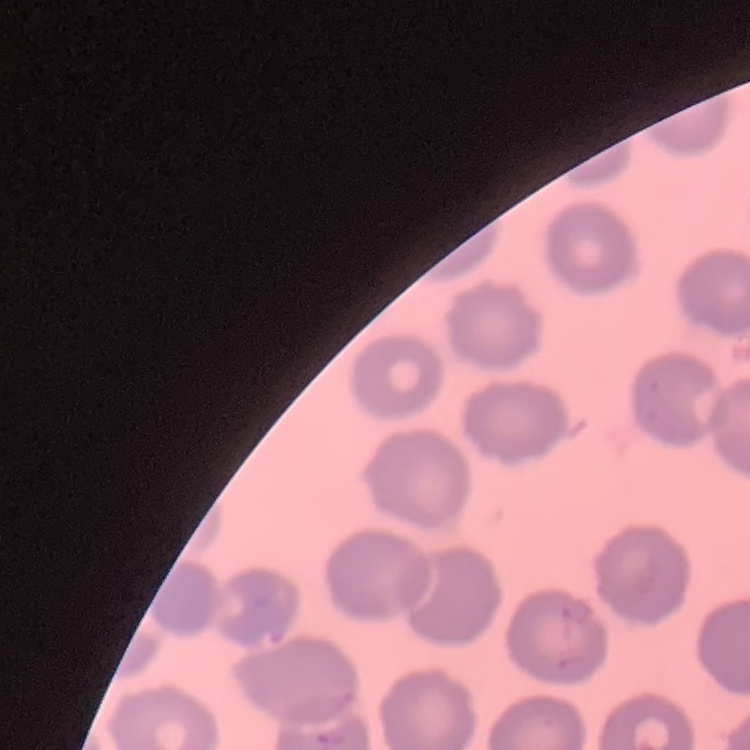
{
  "red_blood_cell_morphology": "no rouleaux formation",
  "stain": "Field's or Giemsa",
  "preparation": "thin peripheral smear",
  "image_type": "square crop of a larger photomicrograph"
}